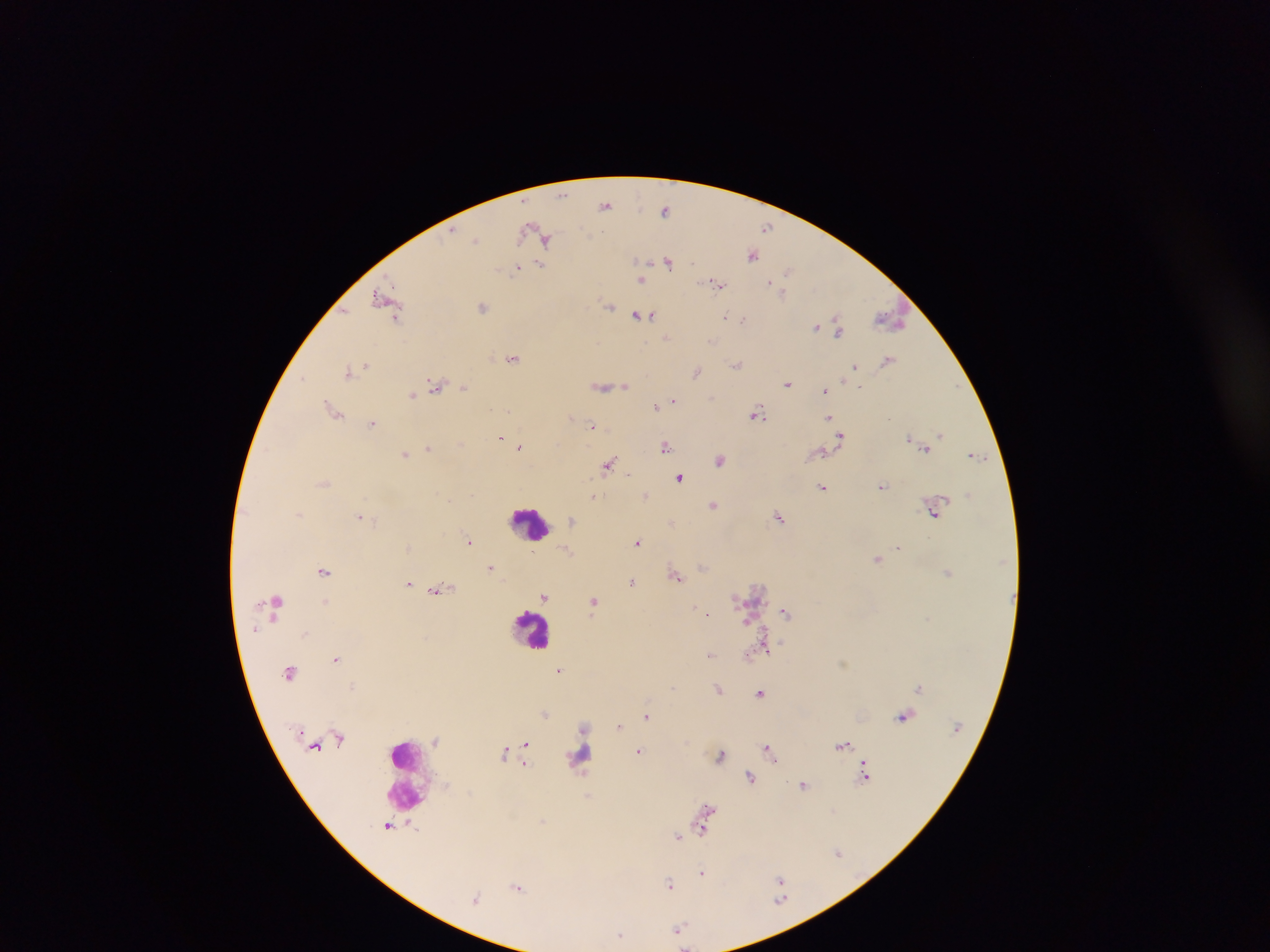
preparation: thick blood smear
leukocyte_locations: 'approximate centers as {x, y} in pixels: {531, 523}, {532, 628}, {406, 771}'
image_size: 1270×952 pixels
capture: mobile-phone photograph through a microscope
country: Ghana
field_of_view: single
plasmodium_parasite_locations: 'approximate centers as {x, y} in pixels: {562, 195}, {605, 205}, {665, 208}, {767, 227}, {476, 239}, {546, 240}, {752, 255}, {668, 261}, {539, 265}, {516, 269}, {788, 272}, {642, 280}, {771, 283}, {717, 284}, {781, 291}, {382, 298}, {609, 305}, {482, 306}, {639, 314}, {650, 315}, {725, 316}, {395, 317}, {743, 319}, {891, 319}, {816, 327}, {838, 329}, {666, 337}, {711, 341}, {513, 358}, {888, 360}, {737, 364}, {363, 366}, {357, 368}, {855, 368}, {348, 371}, {696, 372}, {303, 377}, {787, 383}, {436, 385}, {603, 386}, {624, 386}, {464, 387}, {860, 387}, {825, 389}, {412, 396}, {711, 398}, {674, 400}, {655, 407}, {333, 409}, {758, 414}, {571, 415}, {829, 417}, {889, 418}, {373, 423}, {592, 425}, {940, 434}, {841, 436}, {501, 438}, {908, 439}, {914, 442}, {664, 446}, {519, 447}, {428, 448}, {925, 448}, {822, 452}, {405, 454}, {975, 454}, {720, 460}, {609, 464}, {628, 474}, {679, 478}, {883, 486}, {823, 487}, {595, 496}, {645, 496}, {713, 505}, {934, 510}, {359, 516}, {778, 517}, {571, 519}, {672, 523}, {468, 541}, {638, 542}, {898, 547}, {878, 558}, {491, 567}, {323, 571}, {948, 572}, {676, 574}, {632, 582}, {408, 583}, {439, 589}, {545, 597}, {594, 601}, {325, 602}, {276, 603}, {693, 608}, {785, 612}, {708, 614}, {929, 618}, {255, 629}, {305, 633}, {766, 650}, {710, 654}, {336, 659}, {560, 669}, {290, 672}, {352, 686}, {920, 686}, {673, 687}, {719, 688}, {760, 694}, {545, 714}, {647, 716}, {903, 717}, {619, 726}, {525, 743}, {843, 745}, {768, 750}, {639, 751}, {503, 752}, {721, 755}, {526, 765}, {865, 776}, {751, 777}, {803, 785}, {707, 809}, {388, 826}, {704, 826}, {678, 837}, {838, 852}, {702, 872}, {780, 879}, {669, 884}, {517, 886}, {476, 898}, {781, 899}, {679, 929}, {620, 934}'